Report the malaria status of this cell.
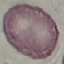

It is uninfected.

preparation = thin smear
capture = smartphone through the microscope eyepiece
image type = cell patch, automatically extracted from a larger field of view and resized to 64 × 64 pixels
stain = Giemsa